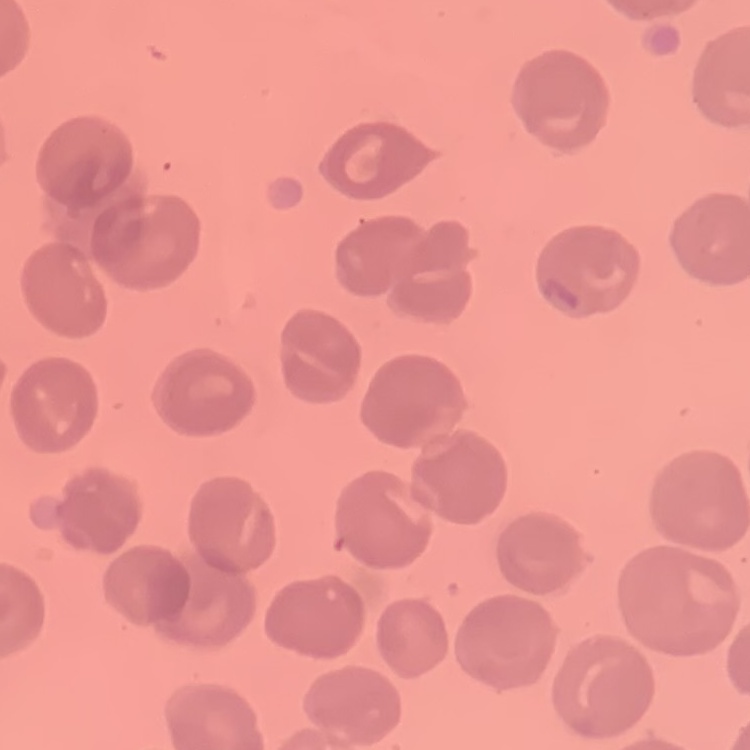

erythrocyte morphology = no rouleaux formation
stain = Field's or Giemsa
preparation = thin peripheral smear
image type = one tile cut from a larger photomicrograph